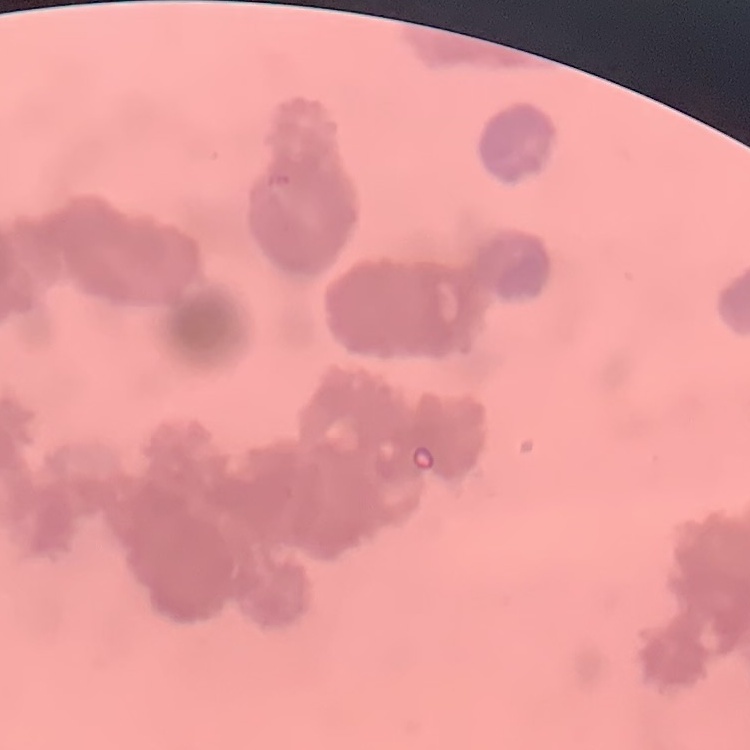
erythrocyte morphology = rouleaux formation
image type = one tile cut from a larger photomicrograph
stain = Field's or Giemsa
preparation = thin blood smear